Identify the blood parasite species.
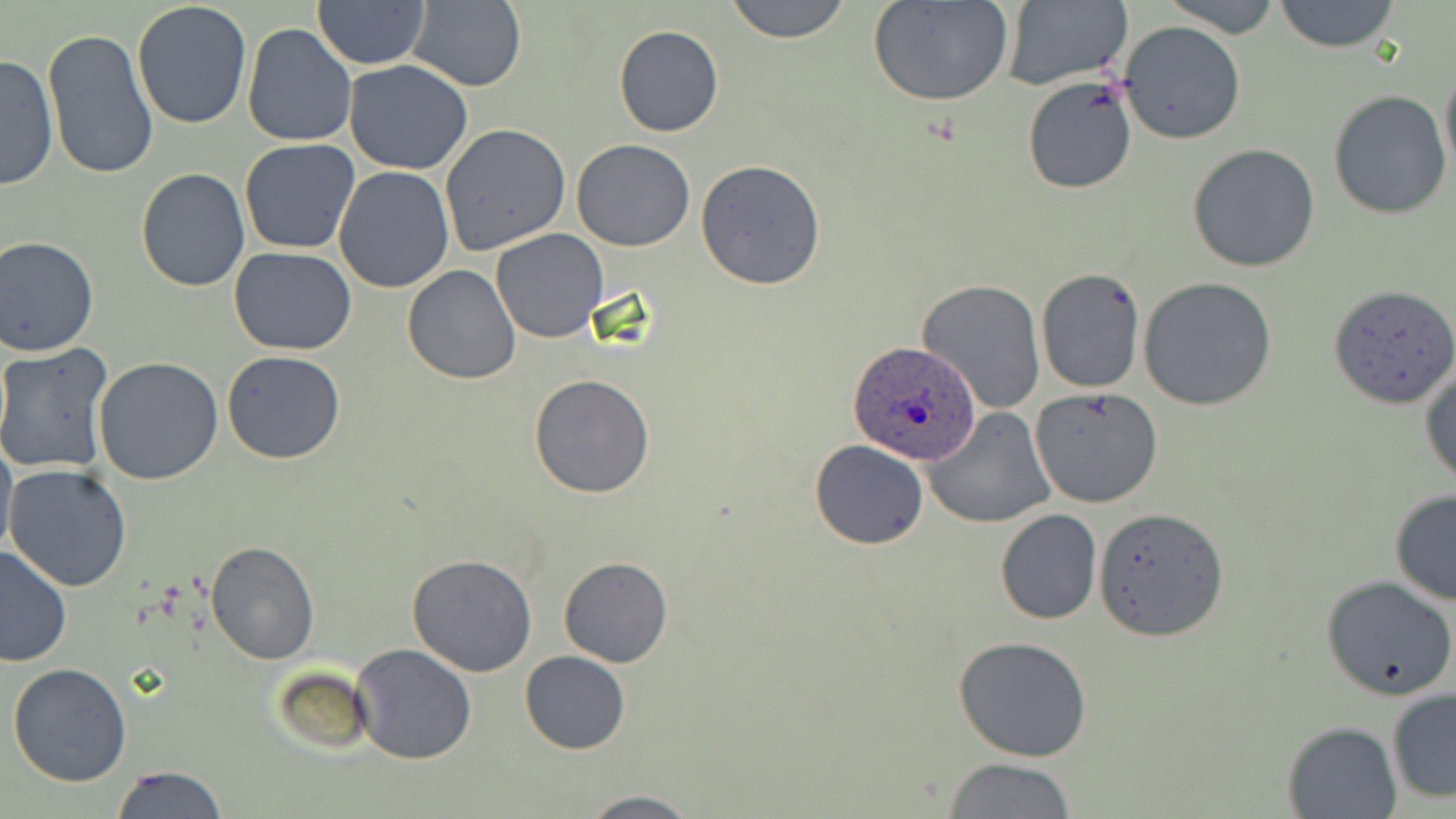
Plasmodium ovale.

{
  "field_of_view": "single",
  "plasmodium_ovale_infected_red_blood_cell_locations_subset": "approximate bounding boxes as named x1/y1/x2/y2 corners in pixels: (x1=848, y1=340, x2=981, y2=463)",
  "image_size": "1456×819 pixels",
  "stain": "May-Grünwald-Giemsa",
  "preparation": "thin blood smear",
  "modality": "optical microscopy",
  "uninfected_red_blood_cell_locations_subset": "approximate bounding boxes as named x1/y1/x2/y2 corners in pixels: (x1=406, y1=0, x2=527, y2=92), (x1=725, y1=0, x2=854, y2=43), (x1=869, y1=0, x2=1014, y2=106), (x1=1000, y1=0, x2=1132, y2=92), (x1=1161, y1=0, x2=1281, y2=36), (x1=1275, y1=0, x2=1400, y2=53), (x1=314, y1=2, x2=428, y2=70), (x1=131, y1=3, x2=253, y2=132), (x1=1119, y1=21, x2=1246, y2=143), (x1=242, y1=24, x2=358, y2=148), (x1=614, y1=25, x2=723, y2=137), (x1=42, y1=28, x2=158, y2=181), (x1=0, y1=52, x2=57, y2=193), (x1=344, y1=59, x2=474, y2=174), (x1=1439, y1=63, x2=1456, y2=183), (x1=1021, y1=76, x2=1139, y2=194), (x1=1328, y1=91, x2=1453, y2=219), (x1=439, y1=121, x2=572, y2=256), (x1=571, y1=138, x2=695, y2=252), (x1=240, y1=139, x2=361, y2=255), (x1=1188, y1=144, x2=1320, y2=272), (x1=694, y1=159, x2=825, y2=290), (x1=333, y1=166, x2=455, y2=295), (x1=135, y1=169, x2=251, y2=293), (x1=491, y1=228, x2=609, y2=343), (x1=0, y1=237, x2=99, y2=356), (x1=230, y1=246, x2=355, y2=355), (x1=403, y1=265, x2=521, y2=384), (x1=1035, y1=267, x2=1144, y2=394), (x1=1139, y1=277, x2=1278, y2=411), (x1=917, y1=280, x2=1046, y2=414), (x1=0, y1=344, x2=114, y2=474), (x1=221, y1=350, x2=345, y2=464), (x1=94, y1=355, x2=224, y2=486), (x1=1420, y1=360, x2=1455, y2=489), (x1=529, y1=375, x2=654, y2=498), (x1=1031, y1=387, x2=1165, y2=509), (x1=924, y1=407, x2=1056, y2=528), (x1=0, y1=433, x2=17, y2=563), (x1=809, y1=440, x2=928, y2=550), (x1=5, y1=464, x2=131, y2=593), (x1=1389, y1=489, x2=1456, y2=605), (x1=1094, y1=508, x2=1227, y2=642), (x1=996, y1=509, x2=1102, y2=624), (x1=205, y1=539, x2=319, y2=664), (x1=0, y1=545, x2=72, y2=667), (x1=407, y1=554, x2=538, y2=677), (x1=558, y1=557, x2=672, y2=667), (x1=1320, y1=575, x2=1455, y2=702), (x1=952, y1=635, x2=1095, y2=761), (x1=350, y1=644, x2=479, y2=766), (x1=520, y1=651, x2=631, y2=754), (x1=6, y1=663, x2=132, y2=787), (x1=271, y1=666, x2=374, y2=757), (x1=1386, y1=689, x2=1456, y2=803), (x1=1282, y1=721, x2=1402, y2=818), (x1=944, y1=757, x2=1079, y2=817), (x1=111, y1=765, x2=227, y2=819), (x1=576, y1=791, x2=703, y2=818)",
  "magnification": "1000x"
}